Assess the morphology of the red blood cells.
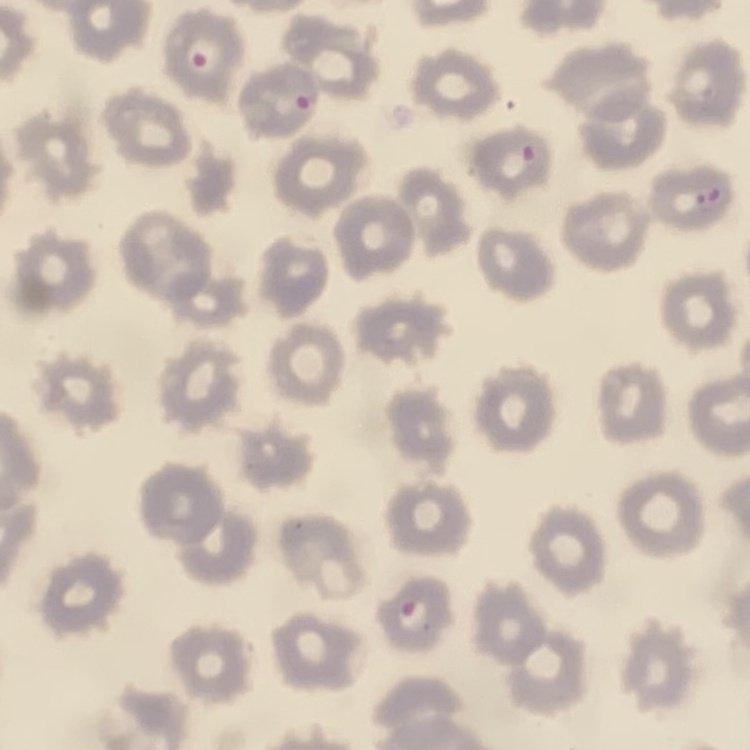
No rouleaux formation.

{
  "preparation": "thin blood film",
  "image_type": "square crop of a larger photomicrograph",
  "stain": "Field's or Giemsa"
}